Name the blood parasite species.
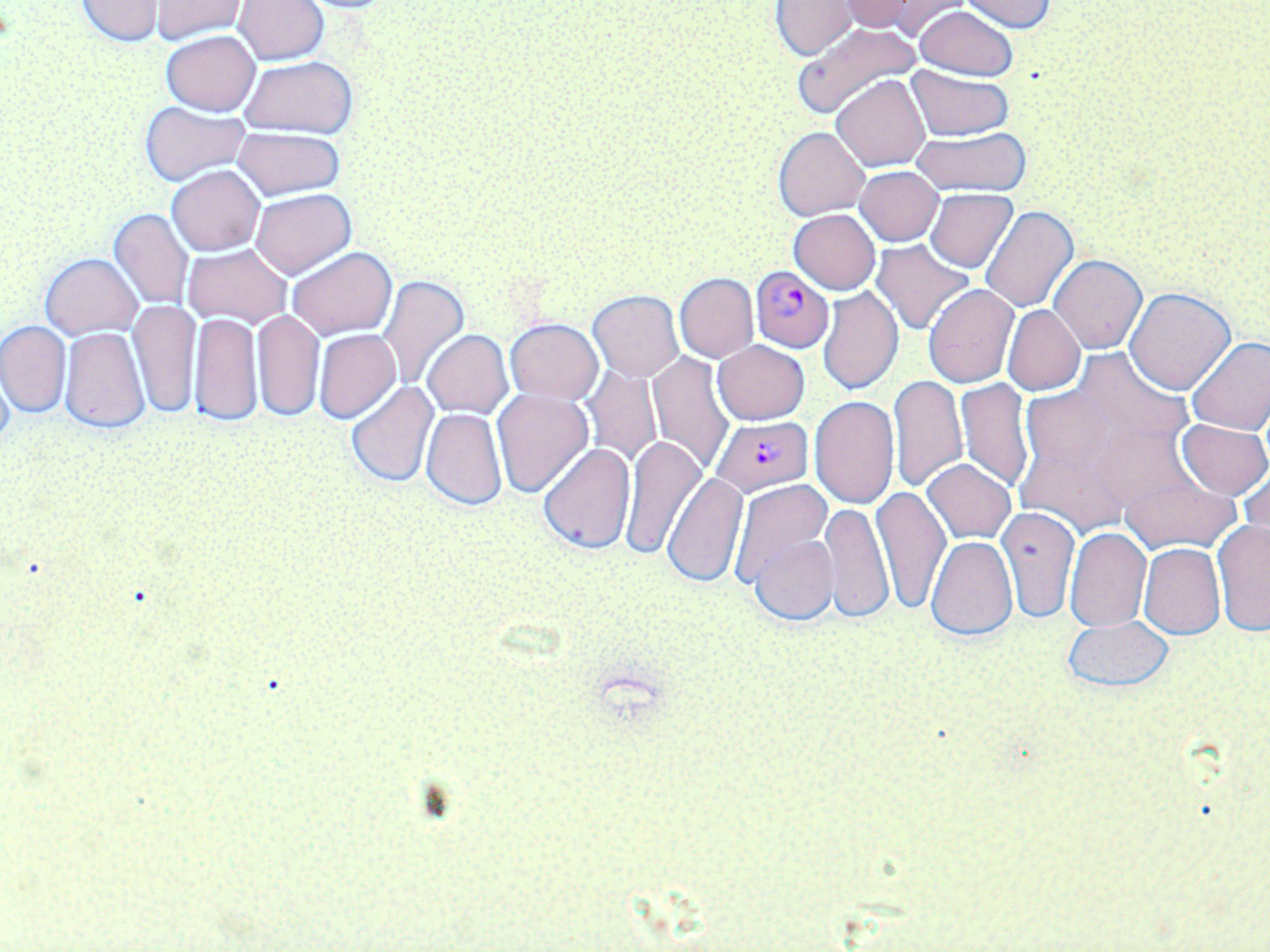

Plasmodium falciparum.

Summary:
  - Coordinate format: approximate bounding boxes as named x1/y1/x2/y2 corners in pixels
  - Plasmodium falciparum-infected red blood cell locations: (x1=749, y1=266, x2=835, y2=353), (x1=711, y1=415, x2=814, y2=496)
  - Uninfected red blood cell locations: (x1=77, y1=0, x2=164, y2=46), (x1=234, y1=0, x2=328, y2=66), (x1=291, y1=0, x2=403, y2=14), (x1=833, y1=0, x2=943, y2=34), (x1=961, y1=0, x2=1059, y2=33), (x1=150, y1=1, x2=247, y2=42), (x1=772, y1=1, x2=860, y2=59), (x1=914, y1=6, x2=1018, y2=80), (x1=792, y1=21, x2=922, y2=118), (x1=161, y1=31, x2=260, y2=115), (x1=240, y1=56, x2=357, y2=137), (x1=907, y1=67, x2=1013, y2=140), (x1=832, y1=74, x2=931, y2=171), (x1=139, y1=102, x2=250, y2=186), (x1=233, y1=126, x2=345, y2=201), (x1=774, y1=126, x2=871, y2=219), (x1=910, y1=128, x2=1031, y2=195), (x1=167, y1=165, x2=265, y2=255), (x1=855, y1=166, x2=944, y2=245), (x1=926, y1=187, x2=1017, y2=272), (x1=250, y1=189, x2=356, y2=279), (x1=980, y1=205, x2=1079, y2=311), (x1=109, y1=210, x2=192, y2=310), (x1=789, y1=210, x2=881, y2=294), (x1=872, y1=241, x2=974, y2=336), (x1=184, y1=243, x2=292, y2=328), (x1=287, y1=247, x2=397, y2=340), (x1=40, y1=253, x2=142, y2=339), (x1=1050, y1=255, x2=1145, y2=353), (x1=675, y1=274, x2=758, y2=361), (x1=377, y1=275, x2=469, y2=390), (x1=923, y1=284, x2=1018, y2=388), (x1=818, y1=286, x2=904, y2=395), (x1=1125, y1=288, x2=1234, y2=392), (x1=588, y1=290, x2=684, y2=381), (x1=129, y1=302, x2=200, y2=417), (x1=1002, y1=305, x2=1085, y2=396), (x1=253, y1=310, x2=325, y2=422), (x1=189, y1=311, x2=263, y2=427), (x1=505, y1=319, x2=603, y2=403), (x1=0, y1=321, x2=71, y2=416), (x1=59, y1=327, x2=149, y2=431), (x1=313, y1=330, x2=400, y2=423), (x1=423, y1=331, x2=512, y2=417), (x1=1187, y1=336, x2=1270, y2=435), (x1=713, y1=342, x2=809, y2=424), (x1=646, y1=353, x2=733, y2=474), (x1=580, y1=368, x2=661, y2=465), (x1=889, y1=373, x2=967, y2=492), (x1=955, y1=378, x2=1035, y2=490), (x1=345, y1=380, x2=438, y2=487), (x1=491, y1=388, x2=592, y2=498), (x1=808, y1=395, x2=899, y2=509), (x1=421, y1=407, x2=507, y2=509), (x1=1014, y1=417, x2=1146, y2=536), (x1=1177, y1=418, x2=1270, y2=500), (x1=618, y1=436, x2=705, y2=558), (x1=537, y1=443, x2=636, y2=553), (x1=922, y1=459, x2=1016, y2=544), (x1=1239, y1=463, x2=1269, y2=555), (x1=664, y1=473, x2=747, y2=588), (x1=1121, y1=474, x2=1239, y2=554), (x1=727, y1=478, x2=833, y2=588), (x1=871, y1=486, x2=950, y2=613), (x1=821, y1=502, x2=893, y2=624), (x1=998, y1=505, x2=1079, y2=622), (x1=1212, y1=518, x2=1270, y2=637), (x1=1065, y1=527, x2=1151, y2=630), (x1=750, y1=537, x2=836, y2=626), (x1=927, y1=537, x2=1017, y2=642), (x1=1138, y1=544, x2=1224, y2=638), (x1=1063, y1=614, x2=1174, y2=694)
  - Modality: light microscopy
  - Field of view: single
  - Magnification: 1000x
  - Preparation: thin blood smear
  - Stain: May-Grünwald-Giemsa
  - Image size: 1270×952 pixels